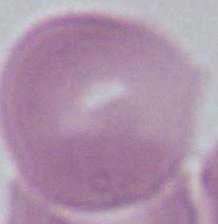 Captured at 1000x magnification. Micrograph. A red blood cell is seen.